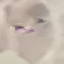
result = no malaria parasites seen
stain = Giemsa
preparation = thin smear
image type = cell patch, automatically extracted from a larger field of view and resized to 64 × 64 pixels
capture = smartphone camera at the microscope eyepiece